Name the parasite shown.
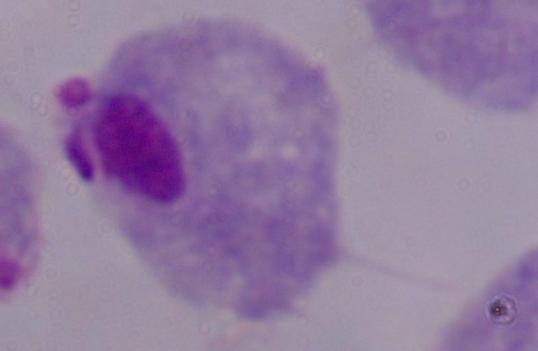

This is a trichomonad.

modality = photomicrograph
magnification = 1000x